Report the malaria status.
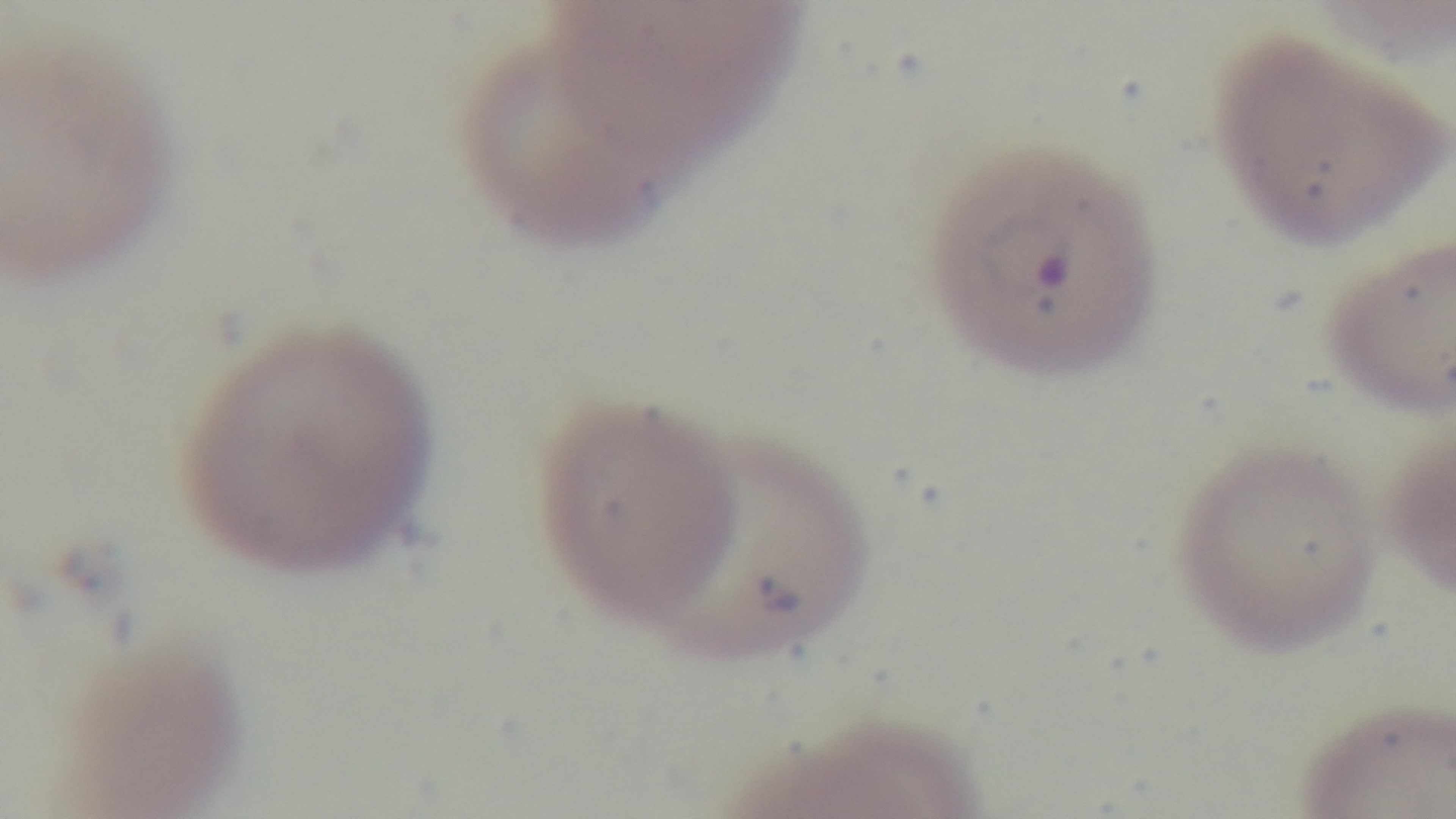

Infected.

Giemsa-stained. Single field of view. 100x oil-immersion objective. Light microscopy. Mounted 4K digital camera. Preparation: thin blood film.